Classify this cell by malaria status.
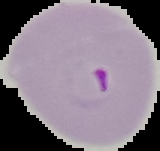
Parasitized.

From a thin blood smear. Image is 160×151 pixels. Cell region segmented out of the field of view; the surrounding area is masked to black.